Comment on the morphology of the erythrocytes.
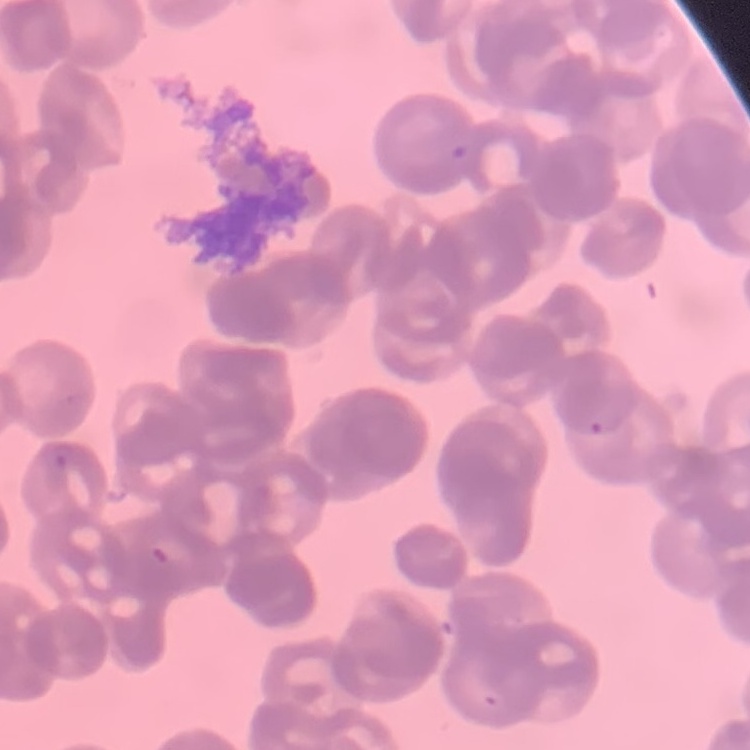
They show rouleaux formation.

Summary:
  - Preparation: thin peripheral smear
  - Stain: Field's or Giemsa
  - Image type: one tile cut from a larger photomicrograph